Assess this cell for malaria.
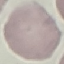

Uninfected.

Summary:
  - Capture: smartphone camera at the microscope eyepiece
  - Stain: Giemsa
  - Image type: automatically extracted cell patch, resized to 64 × 64 pixels
  - Preparation: thin blood smear